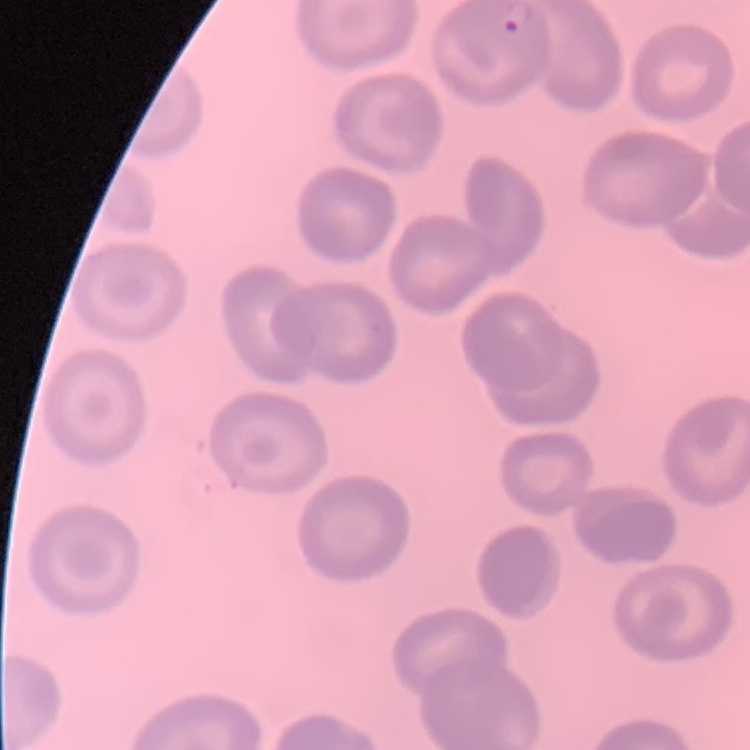

{
  "erythrocyte_morphology": "no rouleaux formation",
  "stain": "Field's or Giemsa",
  "preparation": "thin peripheral smear",
  "image_type": "square crop of a larger photomicrograph"
}